Classify this cell by malaria status.
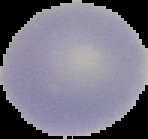

It is uninfected.

image type = segmented cell region with the area outside set to black
preparation = thin blood film
image size = 148×139 pixels